State which cell type is depicted.
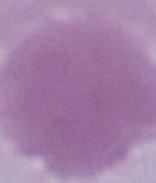

This is an erythrocyte.

{
  "magnification": "1000x",
  "modality": "photomicrograph"
}